Assess the morphology of the erythrocytes.
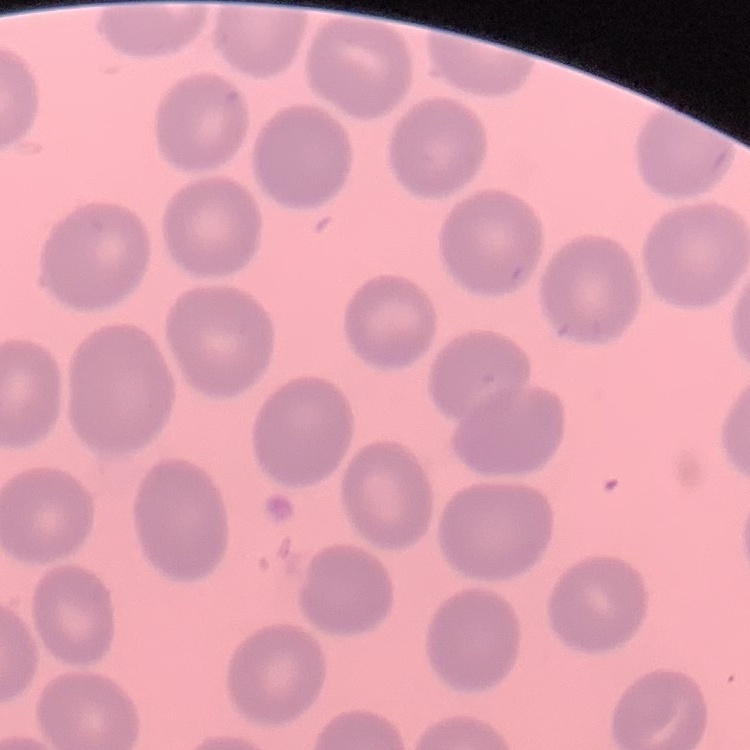
No rouleaux formation.

{
  "stain": "Field's or Giemsa",
  "image_type": "one tile cut from a larger photomicrograph",
  "preparation": "thin peripheral smear"
}